Outline each blood parasite and name the species.
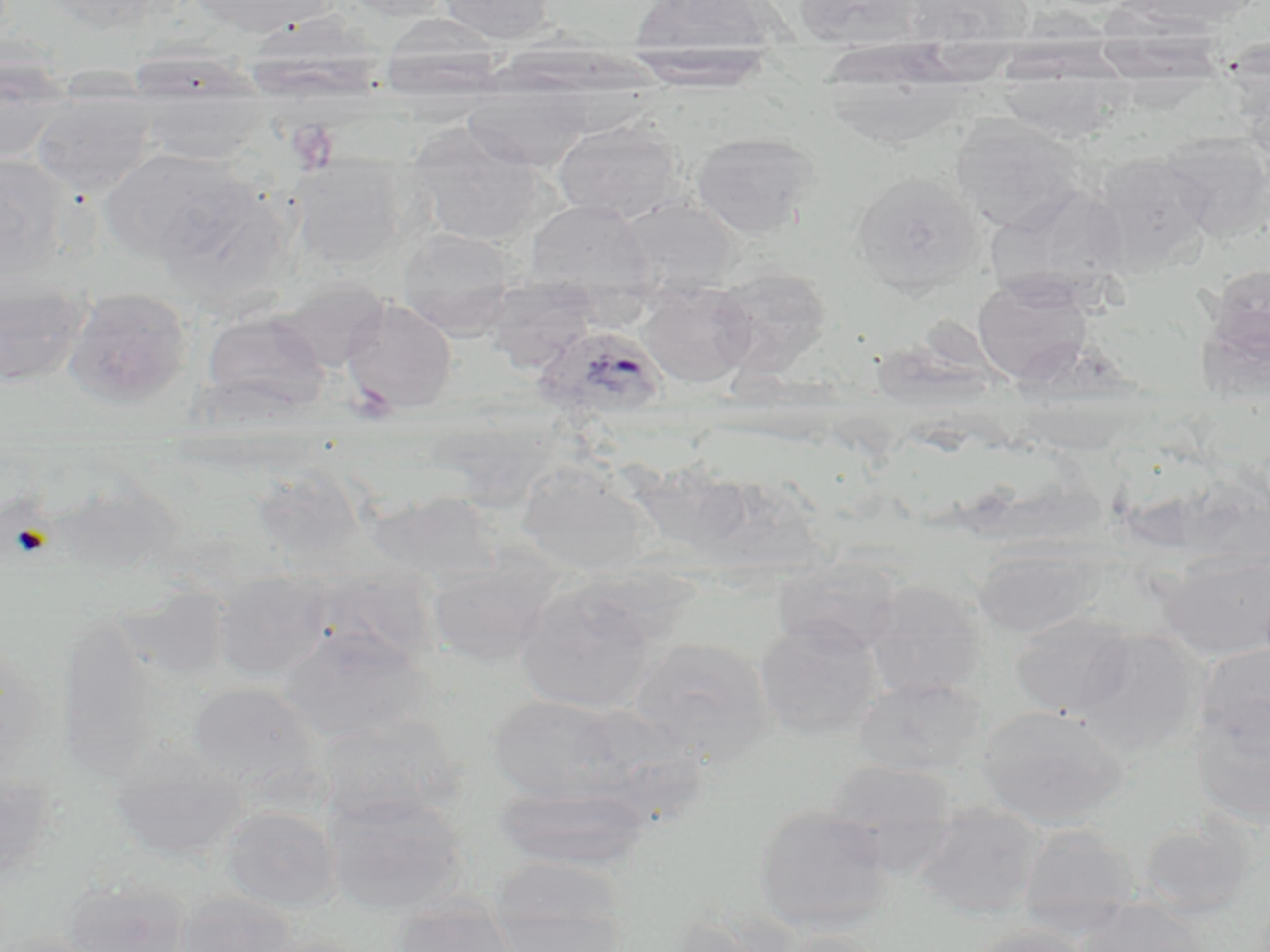

Approximate bounding boxes as named x1/y1/x2/y2 corners in pixels.
Plasmodium ovale-infected red blood cells: (x1=535, y1=326, x2=668, y2=423).
No Plasmodium falciparum, Plasmodium malariae, Plasmodium vivax, Babesia divergens, or Trypanosoma brucei observed.

Summary:
  - Uninfected red blood cell locations: (x1=42, y1=0, x2=162, y2=33), (x1=187, y1=0, x2=334, y2=36), (x1=339, y1=0, x2=454, y2=20), (x1=438, y1=0, x2=555, y2=44), (x1=792, y1=0, x2=925, y2=49), (x1=903, y1=0, x2=1033, y2=47), (x1=1126, y1=0, x2=1257, y2=30), (x1=629, y1=1, x2=783, y2=55), (x1=249, y1=9, x2=400, y2=117), (x1=378, y1=15, x2=505, y2=100), (x1=822, y1=34, x2=970, y2=147), (x1=622, y1=43, x2=779, y2=90), (x1=0, y1=57, x2=72, y2=164), (x1=139, y1=79, x2=266, y2=164), (x1=464, y1=88, x2=591, y2=170), (x1=31, y1=91, x2=153, y2=197), (x1=950, y1=115, x2=1083, y2=231), (x1=552, y1=120, x2=682, y2=223), (x1=408, y1=126, x2=545, y2=247), (x1=691, y1=132, x2=820, y2=238), (x1=1163, y1=132, x2=1270, y2=242), (x1=99, y1=147, x2=253, y2=265), (x1=1090, y1=152, x2=1213, y2=274), (x1=0, y1=154, x2=71, y2=279), (x1=292, y1=158, x2=406, y2=269), (x1=852, y1=170, x2=983, y2=294), (x1=989, y1=186, x2=1131, y2=300), (x1=615, y1=197, x2=741, y2=298), (x1=526, y1=199, x2=656, y2=302), (x1=398, y1=228, x2=516, y2=337), (x1=1197, y1=265, x2=1270, y2=395), (x1=712, y1=266, x2=831, y2=376), (x1=972, y1=274, x2=1092, y2=386), (x1=0, y1=276, x2=89, y2=388), (x1=484, y1=277, x2=598, y2=373), (x1=276, y1=278, x2=389, y2=373), (x1=639, y1=281, x2=756, y2=388), (x1=63, y1=287, x2=192, y2=406), (x1=341, y1=298, x2=457, y2=414), (x1=200, y1=310, x2=330, y2=417), (x1=455, y1=395, x2=572, y2=510), (x1=517, y1=463, x2=652, y2=578), (x1=684, y1=470, x2=832, y2=577), (x1=367, y1=491, x2=501, y2=582), (x1=973, y1=544, x2=1100, y2=639), (x1=1158, y1=547, x2=1270, y2=661), (x1=771, y1=557, x2=901, y2=656), (x1=426, y1=559, x2=561, y2=666), (x1=212, y1=573, x2=331, y2=681), (x1=514, y1=579, x2=665, y2=715), (x1=864, y1=580, x2=987, y2=700), (x1=1009, y1=612, x2=1137, y2=717), (x1=754, y1=620, x2=885, y2=740), (x1=278, y1=626, x2=432, y2=744), (x1=1074, y1=629, x2=1206, y2=756), (x1=629, y1=636, x2=776, y2=762), (x1=1193, y1=642, x2=1270, y2=756), (x1=855, y1=677, x2=989, y2=775), (x1=188, y1=682, x2=321, y2=793), (x1=486, y1=693, x2=635, y2=804), (x1=975, y1=704, x2=1131, y2=827), (x1=1190, y1=706, x2=1270, y2=828), (x1=315, y1=715, x2=464, y2=830), (x1=109, y1=744, x2=248, y2=862), (x1=822, y1=760, x2=958, y2=858), (x1=0, y1=763, x2=57, y2=882), (x1=493, y1=784, x2=656, y2=870), (x1=324, y1=792, x2=470, y2=917), (x1=754, y1=803, x2=895, y2=922), (x1=909, y1=803, x2=1046, y2=913), (x1=220, y1=805, x2=340, y2=912), (x1=1136, y1=816, x2=1256, y2=917), (x1=1018, y1=826, x2=1138, y2=907), (x1=488, y1=855, x2=629, y2=937), (x1=62, y1=878, x2=193, y2=952), (x1=173, y1=891, x2=299, y2=951), (x1=392, y1=901, x2=520, y2=952), (x1=1014, y1=906, x2=1140, y2=941), (x1=1075, y1=906, x2=1211, y2=952), (x1=669, y1=908, x2=803, y2=952), (x1=486, y1=909, x2=629, y2=952), (x1=963, y1=924, x2=1096, y2=952), (x1=774, y1=931, x2=892, y2=952), (x1=0, y1=932, x2=116, y2=952)
  - Platelet locations: (x1=287, y1=120, x2=339, y2=173), (x1=347, y1=381, x2=398, y2=425)
  - Slide-level diagnosis: Plasmodium ovale
  - Field of view: single
  - Magnification: 1000x
  - Image size: 1270×952 pixels
  - Modality: optical microscopy
  - Stain: May-Grünwald-Giemsa
  - Preparation: thin blood smear